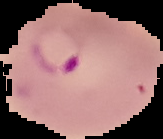

image_type: cell region segmented out of the field of view; surrounding area masked to black
preparation: thin blood film
result: malaria parasites identified
image_size: 163×139 pixels